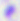

Captured at 400x magnification. Micrograph. Toxoplasma gondii is seen.